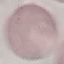
Summary:
  - Malaria status: uninfected
  - Image type: cell patch, automatically extracted from a larger field of view and resized to 64 × 64 pixels
  - Preparation: thin blood smear
  - Stain: Giemsa
  - Capture: smartphone camera at the microscope eyepiece